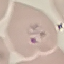

malaria_status: parasitized
capture: smartphone through the microscope eyepiece
preparation: thin smear
image_type: cell patch, automatically extracted from a larger field of view and resized to 64 × 64 pixels
stain: Giemsa